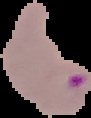

Summary:
  - Image size: 91×118 pixels
  - Malaria status: parasitized
  - Image type: segmented cell region with the area outside set to black
  - Preparation: thin blood smear